Describe the morphology of the red blood cells.
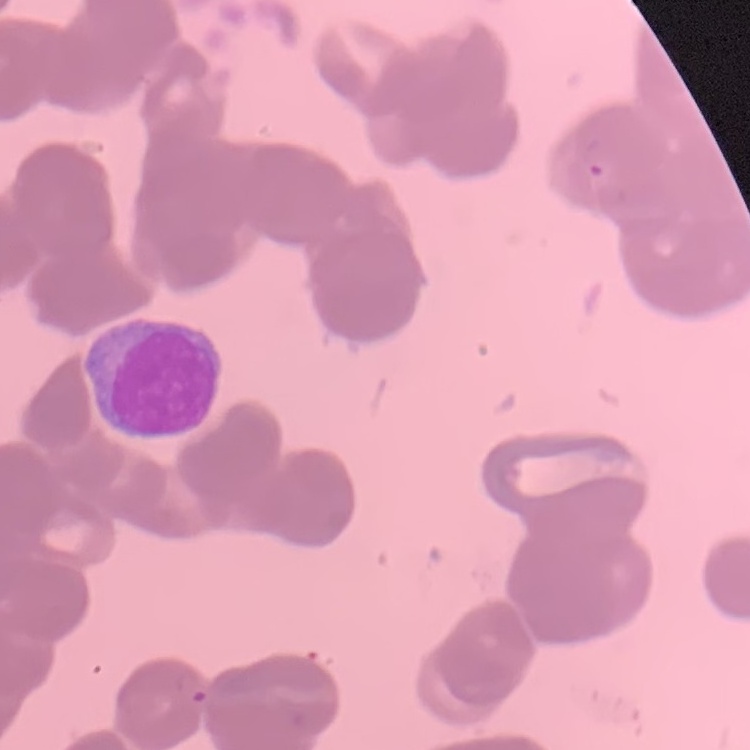

Rouleaux formation.

Field's or Giemsa stain. Square crop of a larger photomicrograph. Thin blood film.